Locate every Plasmodium parasite.
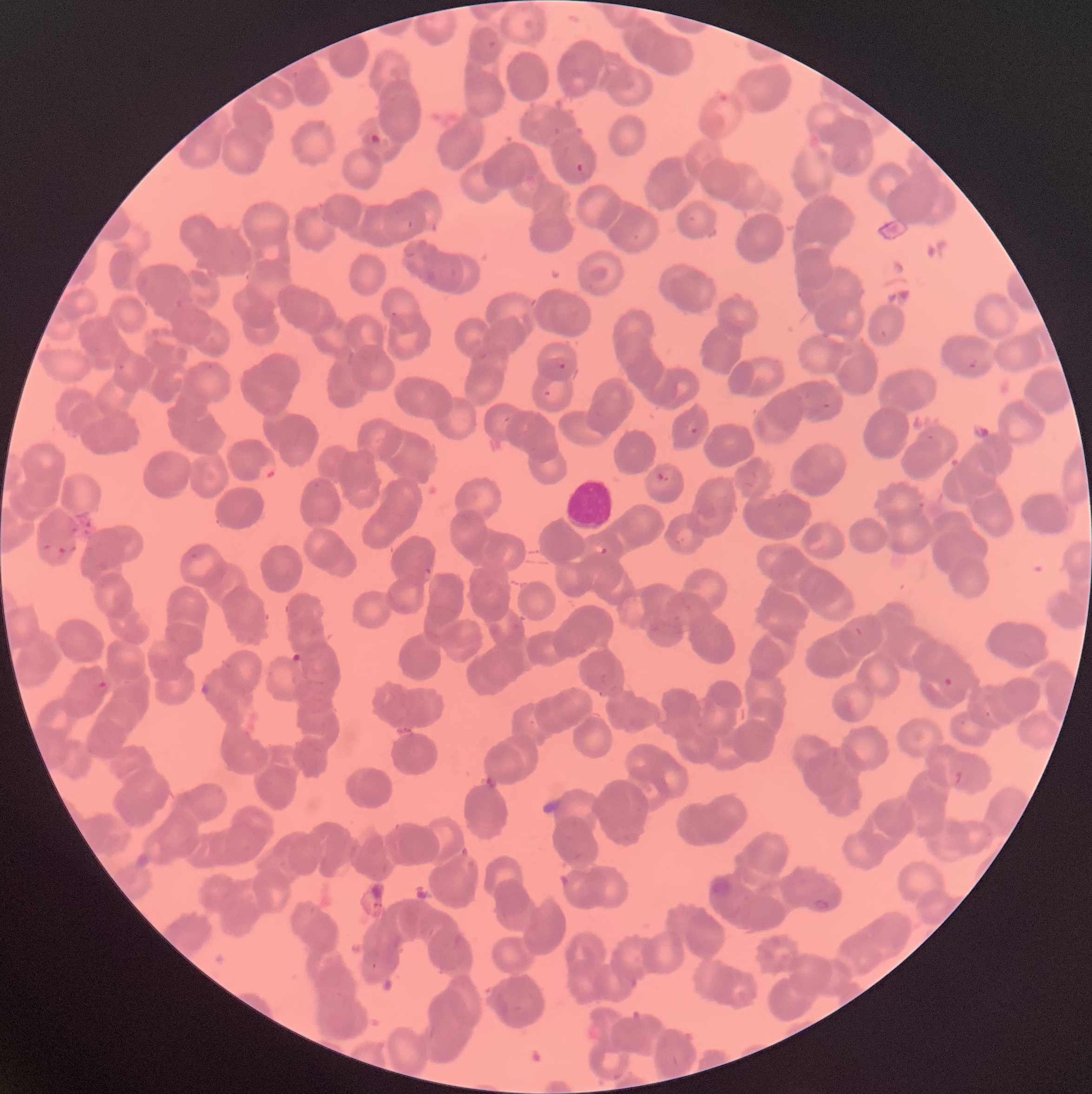

Approximate bounding boxes as [x1, y1, x2, y2] in pixels.
Plasmodium parasites: [573, 162, 594, 178], [390, 311, 398, 318], [967, 357, 978, 369], [557, 363, 567, 370], [543, 389, 552, 399], [689, 426, 700, 437], [256, 462, 278, 480], [656, 471, 669, 483], [674, 537, 685, 544], [597, 545, 608, 555], [184, 549, 208, 561], [425, 564, 433, 576], [91, 678, 109, 700], [199, 683, 210, 696], [812, 898, 830, 910].

Summary:
  - White blood cell locations: [565, 472, 613, 529]
  - Image size: 1092×1094 pixels
  - Modality: optical microscopy
  - Red blood cell morphology: rouleaux formation
  - Preparation: thin blood smear